State which cell type is depicted.
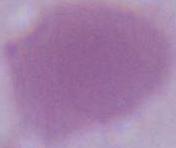
This is an erythrocyte.

Photomicrograph. 1000x magnification.